Locate every blood parasite and identify its species.
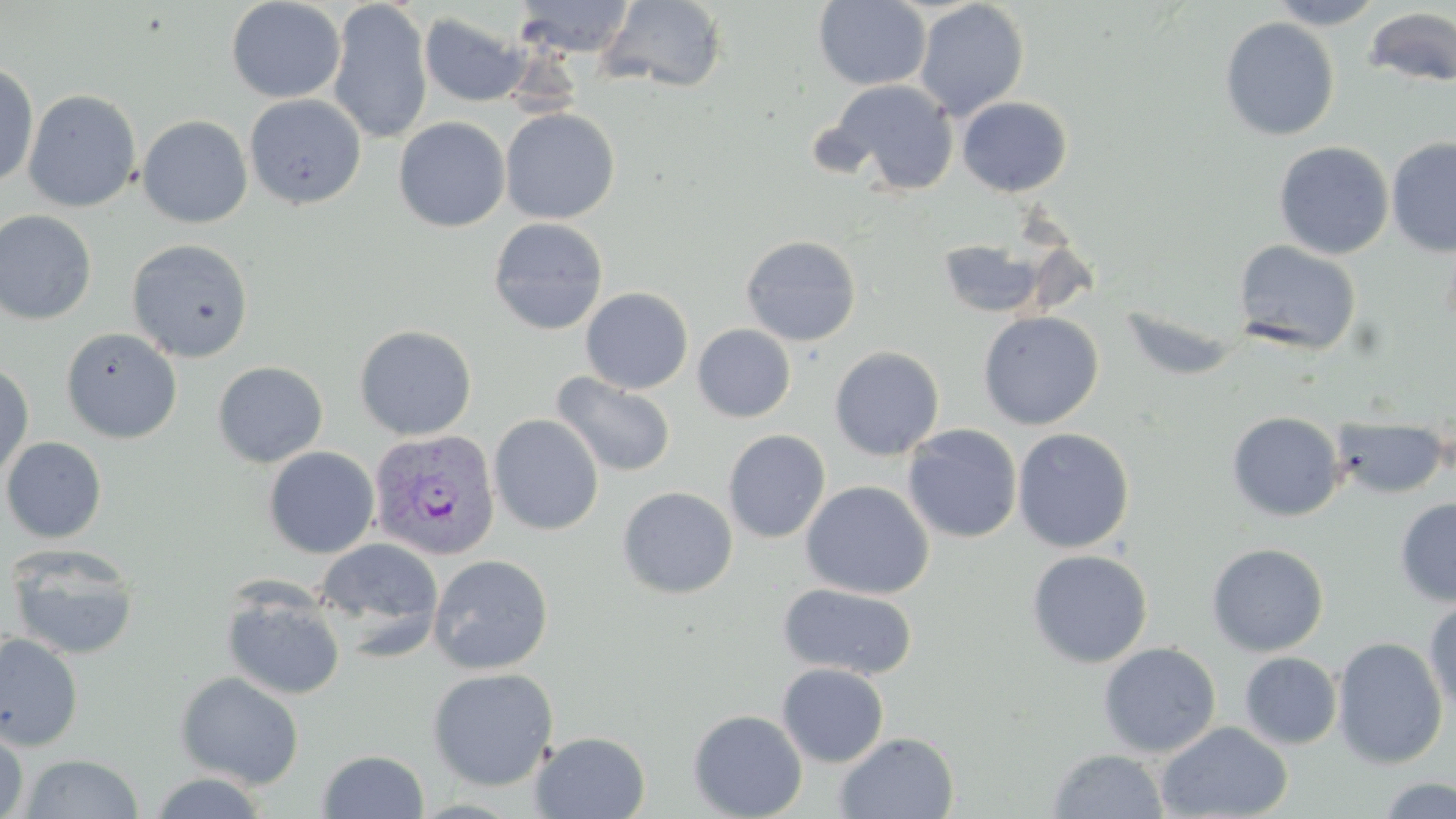
Approximate bounding boxes as (x1,y1)-(x2,y2) corner pairs in pixels.
Plasmodium vivax-infected red blood cells: (370,428)-(500,560).
No Plasmodium falciparum, Plasmodium ovale, Plasmodium malariae, Babesia divergens, or Trypanosoma brucei observed.

Uninfected red blood cell locations: (226,0)-(346,103), (328,0)-(433,144), (512,0)-(637,58), (598,0)-(729,92), (813,0)-(931,90), (1266,0)-(1388,29), (913,1)-(1030,120), (1362,6)-(1456,89), (419,11)-(530,108), (1219,17)-(1340,141), (0,61)-(39,188), (830,80)-(960,196), (22,89)-(141,212), (244,94)-(366,209), (956,96)-(1073,197), (500,108)-(619,224), (137,115)-(253,228), (393,116)-(510,232), (1386,136)-(1456,256), (1274,141)-(1394,260), (0,209)-(98,325), (487,217)-(609,336), (740,234)-(862,346), (935,238)-(1050,319), (126,239)-(253,362), (1233,240)-(1361,355), (580,287)-(693,394), (1118,304)-(1249,382), (977,311)-(1103,430), (354,324)-(477,440), (692,324)-(796,423), (60,327)-(182,444), (829,346)-(945,461), (212,361)-(328,468), (0,363)-(34,483), (551,372)-(676,478), (1226,411)-(1345,521), (488,414)-(604,536), (1332,417)-(1451,498), (902,424)-(1022,543), (1012,427)-(1135,554), (723,430)-(831,543), (1,437)-(106,543), (263,446)-(380,559), (800,480)-(935,600), (617,486)-(738,599), (1395,496)-(1456,606), (315,537)-(444,650), (1206,543)-(1329,656), (6,544)-(140,661), (1026,549)-(1153,668), (428,554)-(553,674), (778,583)-(918,680), (221,587)-(346,701), (1424,596)-(1456,717), (0,633)-(83,751), (1332,636)-(1448,769), (1098,642)-(1221,758), (1240,651)-(1342,750), (777,663)-(889,767), (427,667)-(559,791), (175,672)-(305,789), (687,709)-(808,819), (1156,721)-(1293,819), (0,722)-(29,819), (530,731)-(650,818), (834,731)-(959,818), (1046,749)-(1169,818), (316,750)-(430,818), (19,753)-(143,818), (146,771)-(271,818), (1375,775)-(1456,818). Slide-level diagnosis: Plasmodium vivax. May-Grünwald-Giemsa stain. Captured at 1000x magnification. Single field of view. Image is 1456×819 pixels. Optical microscopy. Thin blood film.